Comment on the morphology of the erythrocytes.
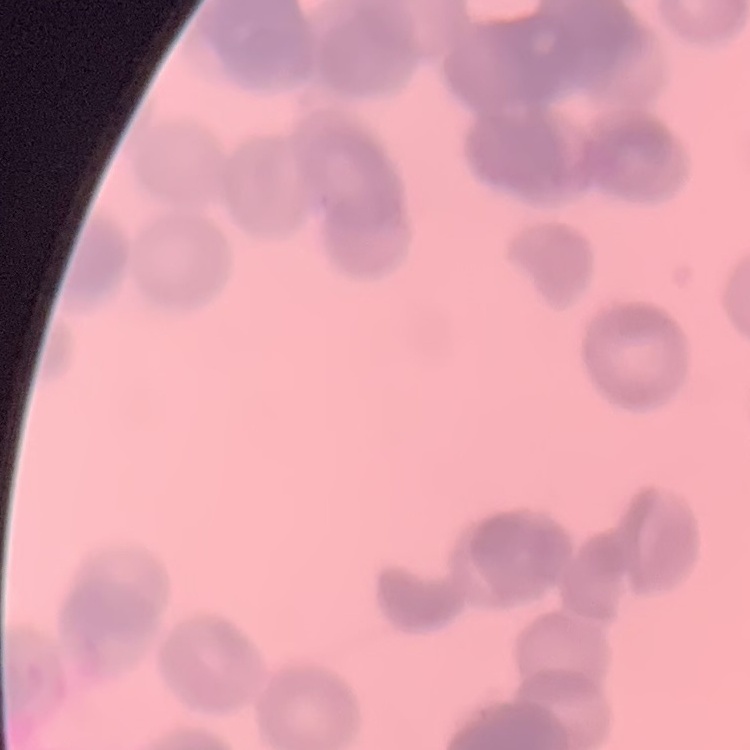

They show rouleaux formation.

Square crop of a larger photomicrograph. Thin peripheral smear. Stained with either Field's or Giemsa.